Locate every malaria parasite.
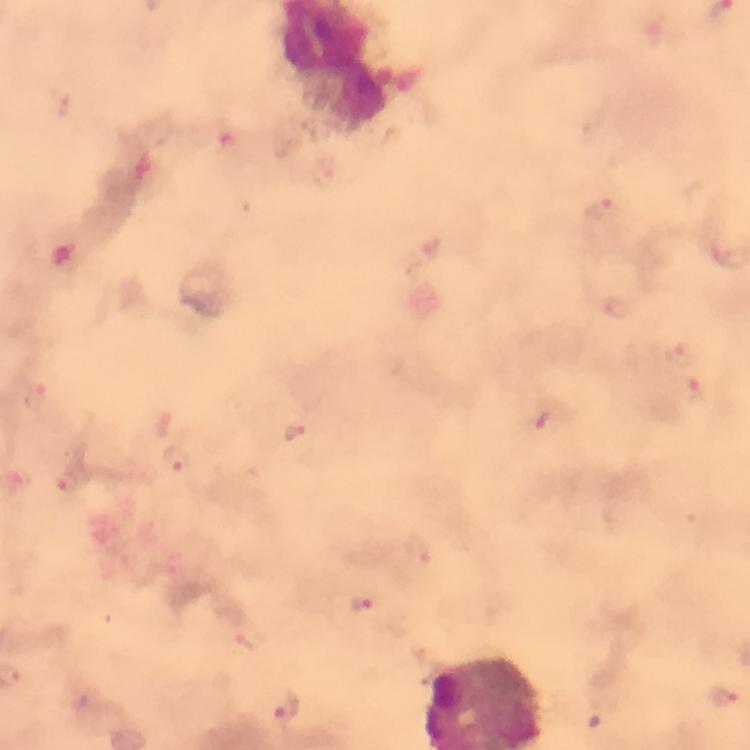
Approximate centers as {x, y} in pixels.
Malaria parasites: {598, 207}, {429, 246}, {617, 307}, {683, 353}, {699, 394}, {35, 397}, {296, 431}, {177, 460}, {67, 484}, {417, 552}, {359, 606}, {251, 639}, {723, 695}, {286, 710}.

{
  "capture": "smartphone photograph through a microscope",
  "preparation": "thick blood film",
  "context": "from a diagnostic examination for malaria",
  "stain": "Giemsa",
  "cropped_from": "one field of view",
  "immersion_oil": "used",
  "image_size": "750×750 pixels",
  "magnification": "100x"
}